Give the extent of all Plasmodium malariae-infected red blood cells.
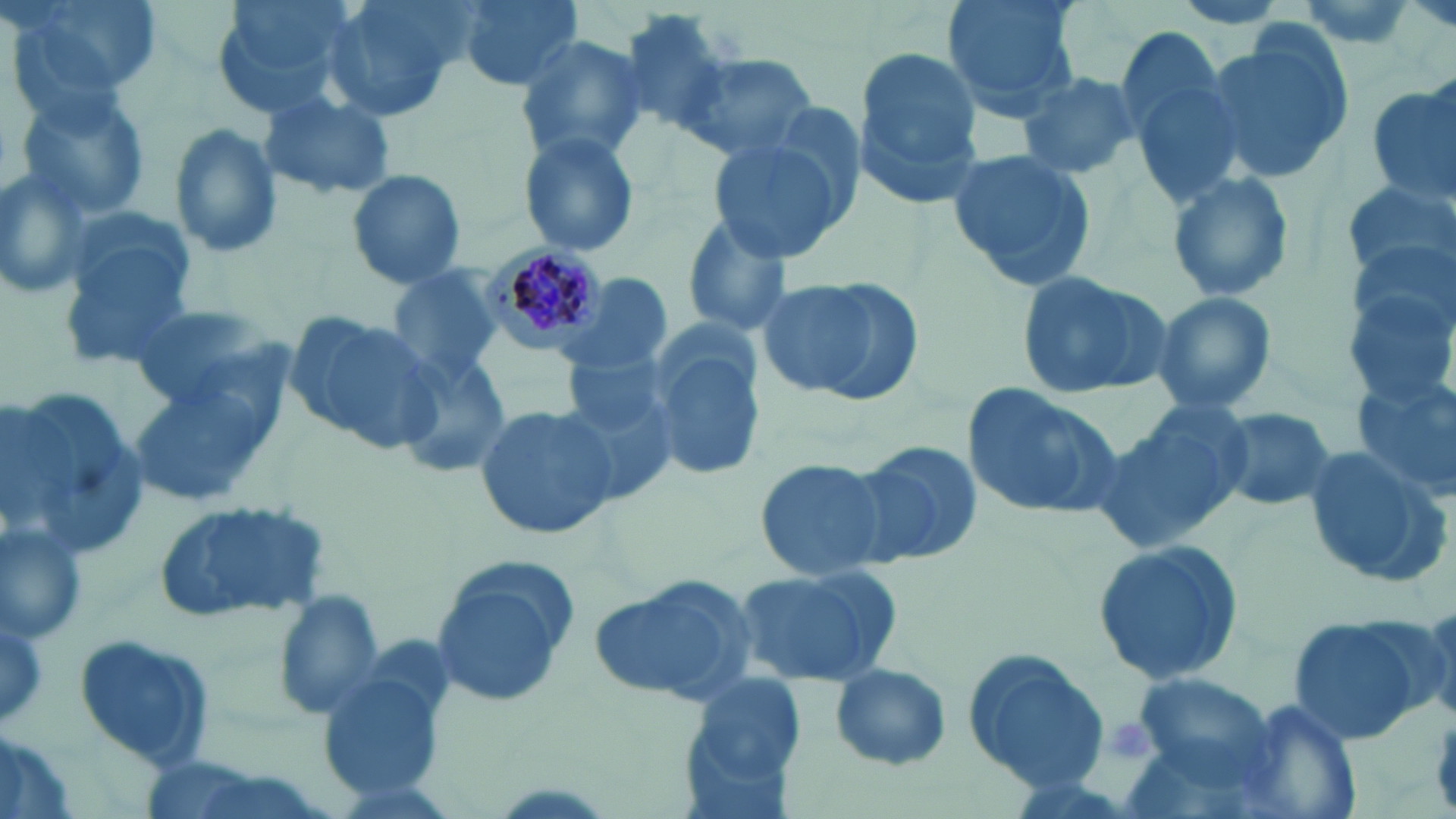
Approximate bounding boxes as named x1/y1/x2/y2 corners in pixels.
Plasmodium malariae-infected red blood cells: (x1=487, y1=244, x2=605, y2=356).

Summary:
  - Uninfected red blood cell locations: (x1=5, y1=0, x2=158, y2=120), (x1=211, y1=0, x2=359, y2=121), (x1=320, y1=0, x2=463, y2=123), (x1=452, y1=0, x2=583, y2=91), (x1=941, y1=0, x2=1083, y2=119), (x1=1404, y1=1, x2=1456, y2=32), (x1=1202, y1=27, x2=1354, y2=188), (x1=1120, y1=30, x2=1246, y2=204), (x1=511, y1=33, x2=651, y2=165), (x1=850, y1=45, x2=986, y2=207), (x1=687, y1=54, x2=821, y2=163), (x1=1018, y1=73, x2=1142, y2=180), (x1=1367, y1=81, x2=1456, y2=205), (x1=17, y1=87, x2=153, y2=223), (x1=260, y1=90, x2=396, y2=201), (x1=709, y1=119, x2=858, y2=263), (x1=167, y1=120, x2=284, y2=261), (x1=517, y1=129, x2=642, y2=261), (x1=946, y1=150, x2=1098, y2=290), (x1=0, y1=166, x2=94, y2=303), (x1=347, y1=168, x2=466, y2=292), (x1=1163, y1=171, x2=1297, y2=305), (x1=1339, y1=178, x2=1453, y2=280), (x1=676, y1=212, x2=798, y2=340), (x1=57, y1=213, x2=193, y2=360), (x1=1344, y1=256, x2=1452, y2=391), (x1=389, y1=265, x2=504, y2=383), (x1=1018, y1=270, x2=1174, y2=397), (x1=561, y1=273, x2=672, y2=377), (x1=755, y1=273, x2=924, y2=406), (x1=1150, y1=290, x2=1278, y2=418), (x1=128, y1=300, x2=278, y2=414), (x1=285, y1=306, x2=444, y2=455), (x1=647, y1=325, x2=766, y2=481), (x1=561, y1=348, x2=675, y2=454), (x1=397, y1=349, x2=513, y2=478), (x1=124, y1=361, x2=293, y2=512), (x1=1352, y1=370, x2=1456, y2=498), (x1=960, y1=380, x2=1125, y2=523), (x1=3, y1=385, x2=148, y2=562), (x1=1098, y1=399, x2=1253, y2=552), (x1=474, y1=403, x2=620, y2=542), (x1=1211, y1=404, x2=1337, y2=512), (x1=846, y1=440, x2=985, y2=570), (x1=1299, y1=444, x2=1451, y2=587), (x1=753, y1=457, x2=892, y2=581), (x1=153, y1=497, x2=331, y2=626), (x1=0, y1=524, x2=88, y2=645), (x1=1093, y1=539, x2=1245, y2=689), (x1=429, y1=562, x2=578, y2=711), (x1=732, y1=562, x2=901, y2=686), (x1=587, y1=572, x2=759, y2=706), (x1=276, y1=590, x2=386, y2=720), (x1=1284, y1=612, x2=1434, y2=745), (x1=75, y1=631, x2=218, y2=769), (x1=961, y1=647, x2=1109, y2=792), (x1=318, y1=659, x2=451, y2=803), (x1=828, y1=665, x2=952, y2=772), (x1=683, y1=671, x2=809, y2=798), (x1=1232, y1=699, x2=1364, y2=819), (x1=0, y1=733, x2=85, y2=819)
  - Platelet locations: (x1=1107, y1=720, x2=1156, y2=765)
  - Slide-level diagnosis: Plasmodium malariae
  - Stain: May-Grünwald-Giemsa
  - Field of view: one of a larger specimen
  - Magnification: 1000x
  - Modality: light microscopy
  - Preparation: thin blood smear
  - Image size: 1456×819 pixels